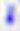
modality = micrograph
identification = Toxoplasma gondii
magnification = 400x